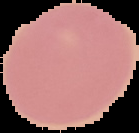

Summary:
  - Preparation: thin blood smear
  - Image size: 139×133 pixels
  - Image type: segmented cell region on a black background
  - Malaria status: uninfected